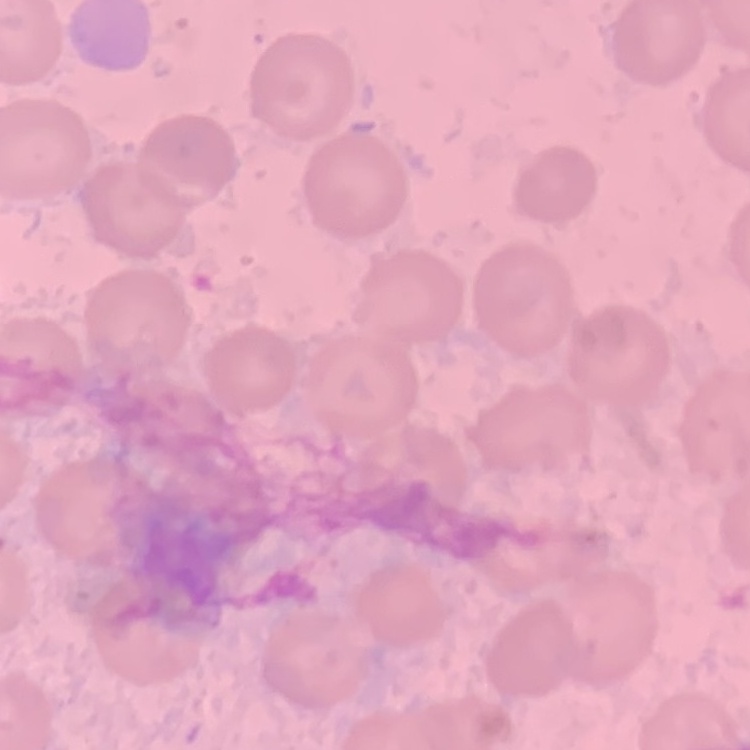

red blood cell morphology = no rouleaux formation
stain = Field's or Giemsa
image type = square crop of a larger photomicrograph
preparation = thin peripheral smear